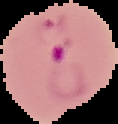

Image is 118×124 pixels. Result: malaria parasites detected. The area outside the segmented cell region is set to black. From a thin blood smear.